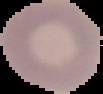
image size = 103×94 pixels
malaria status = uninfected
preparation = thin blood smear
image type = segmented cell region on a black background